Identify the parasite.
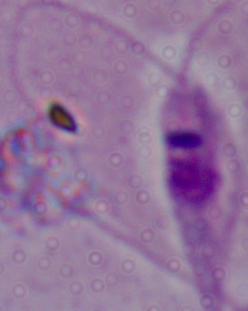
This is Leishmania.

1000x magnification. Photomicrograph.